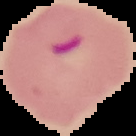

Summary:
  - Image size: 136×136 pixels
  - Preparation: thin blood film
  - Result: malaria parasites detected
  - Image type: segmented cell region on a black background